Locate and identify every blood parasite.
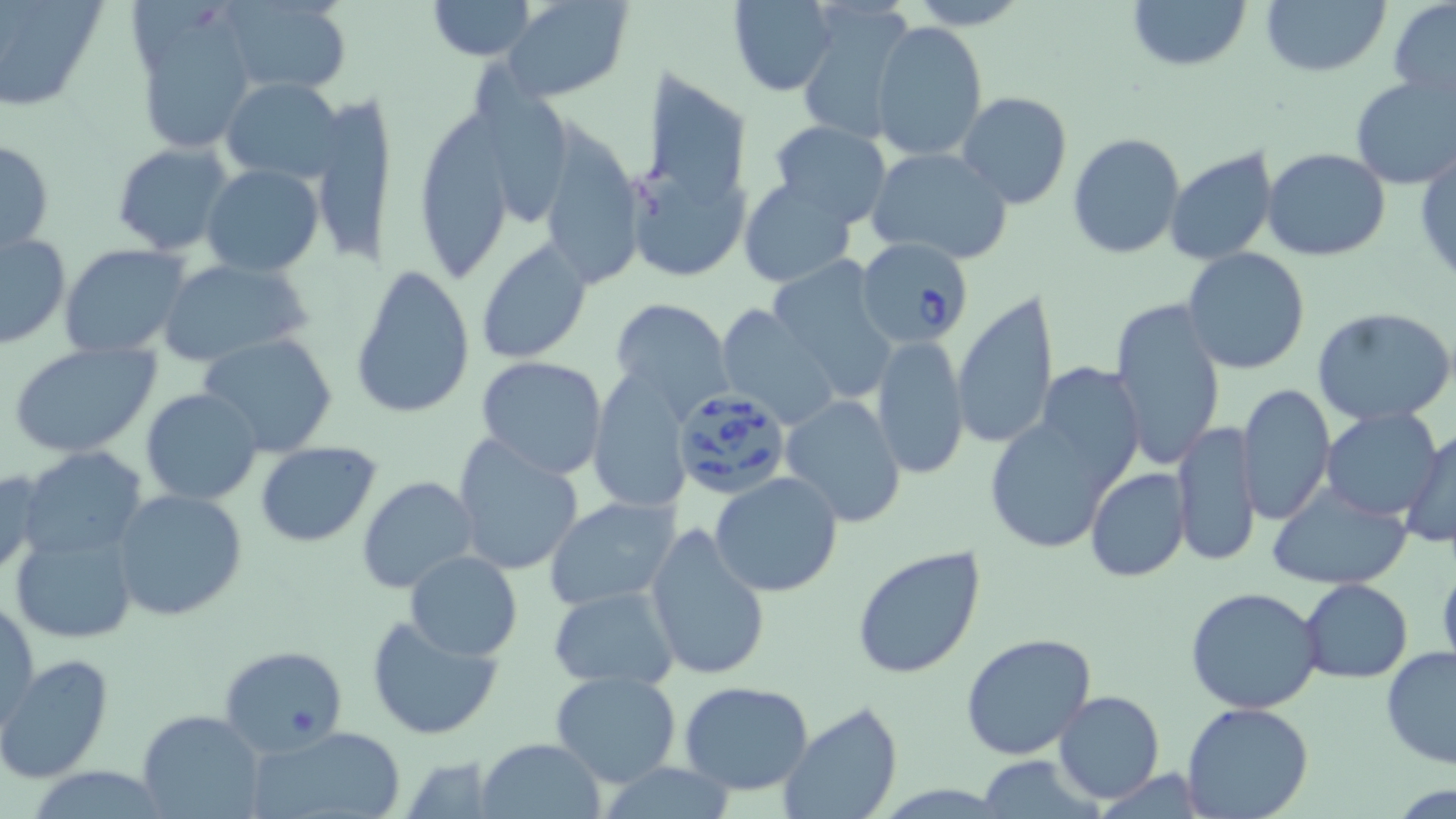

Approximate bounding boxes as [x1, y1, x2, y2] in pixels.
Babesia divergens-infected red blood cells: [855, 237, 973, 345], [667, 387, 794, 501].
No Plasmodium falciparum, Plasmodium ovale, Plasmodium malariae, Plasmodium vivax, or Trypanosoma brucei observed.

Summary:
  - Uninfected red blood cell locations: [0, 0, 104, 111], [217, 0, 353, 95], [426, 0, 537, 60], [503, 0, 632, 101], [1123, 0, 1252, 73], [1262, 0, 1390, 75], [727, 1, 840, 95], [899, 1, 1036, 30], [1388, 1, 1456, 103], [796, 3, 914, 144], [133, 7, 258, 155], [871, 20, 989, 160], [469, 57, 580, 221], [629, 62, 757, 210], [1349, 72, 1456, 191], [223, 77, 344, 183], [956, 91, 1072, 209], [307, 94, 396, 268], [543, 107, 646, 285], [415, 118, 515, 282], [770, 122, 892, 228], [1066, 132, 1184, 260], [0, 140, 54, 255], [111, 141, 234, 256], [1415, 144, 1455, 284], [1163, 146, 1280, 266], [864, 147, 1014, 265], [1262, 148, 1391, 262], [629, 161, 750, 279], [202, 163, 325, 276], [739, 178, 855, 286], [0, 231, 71, 348], [475, 238, 593, 365], [59, 243, 193, 358], [1182, 247, 1310, 374], [156, 257, 313, 368], [766, 257, 899, 399], [351, 264, 474, 419], [954, 288, 1060, 452], [1108, 295, 1227, 469], [607, 297, 733, 420], [716, 303, 840, 429], [1312, 308, 1456, 427], [197, 332, 339, 458], [872, 336, 969, 482], [7, 342, 161, 460], [476, 357, 608, 480], [1034, 367, 1145, 490], [584, 370, 694, 513], [1238, 384, 1335, 523], [139, 387, 263, 506], [781, 394, 907, 527], [986, 395, 1137, 556], [1320, 408, 1444, 520], [1170, 418, 1261, 567], [1404, 429, 1455, 550], [451, 435, 585, 577], [254, 440, 381, 547], [19, 448, 151, 560], [0, 468, 45, 582], [1086, 468, 1190, 582], [710, 472, 843, 595], [357, 475, 480, 594], [1264, 482, 1414, 589], [110, 487, 249, 622], [542, 496, 681, 611], [643, 520, 770, 681], [10, 527, 140, 645], [851, 546, 988, 682], [405, 551, 524, 659], [1436, 559, 1456, 676], [1300, 579, 1414, 682], [547, 583, 679, 690], [1186, 586, 1324, 716], [1, 597, 38, 732], [364, 613, 506, 742], [961, 632, 1099, 759], [218, 644, 349, 755], [1380, 646, 1456, 769], [0, 655, 115, 785], [548, 671, 682, 789], [678, 680, 815, 797], [1053, 690, 1164, 803], [779, 702, 903, 819], [1181, 702, 1316, 819], [138, 710, 263, 818], [248, 725, 403, 819], [476, 737, 605, 818], [400, 755, 500, 818], [977, 758, 1094, 816], [594, 762, 742, 818]
  - Slide-level diagnosis: Babesia divergens
  - Image size: 1456×819 pixels
  - Magnification: 1000x
  - Field of view: single
  - Preparation: thin blood film
  - Modality: optical microscopy
  - Stain: May-Grünwald-Giemsa